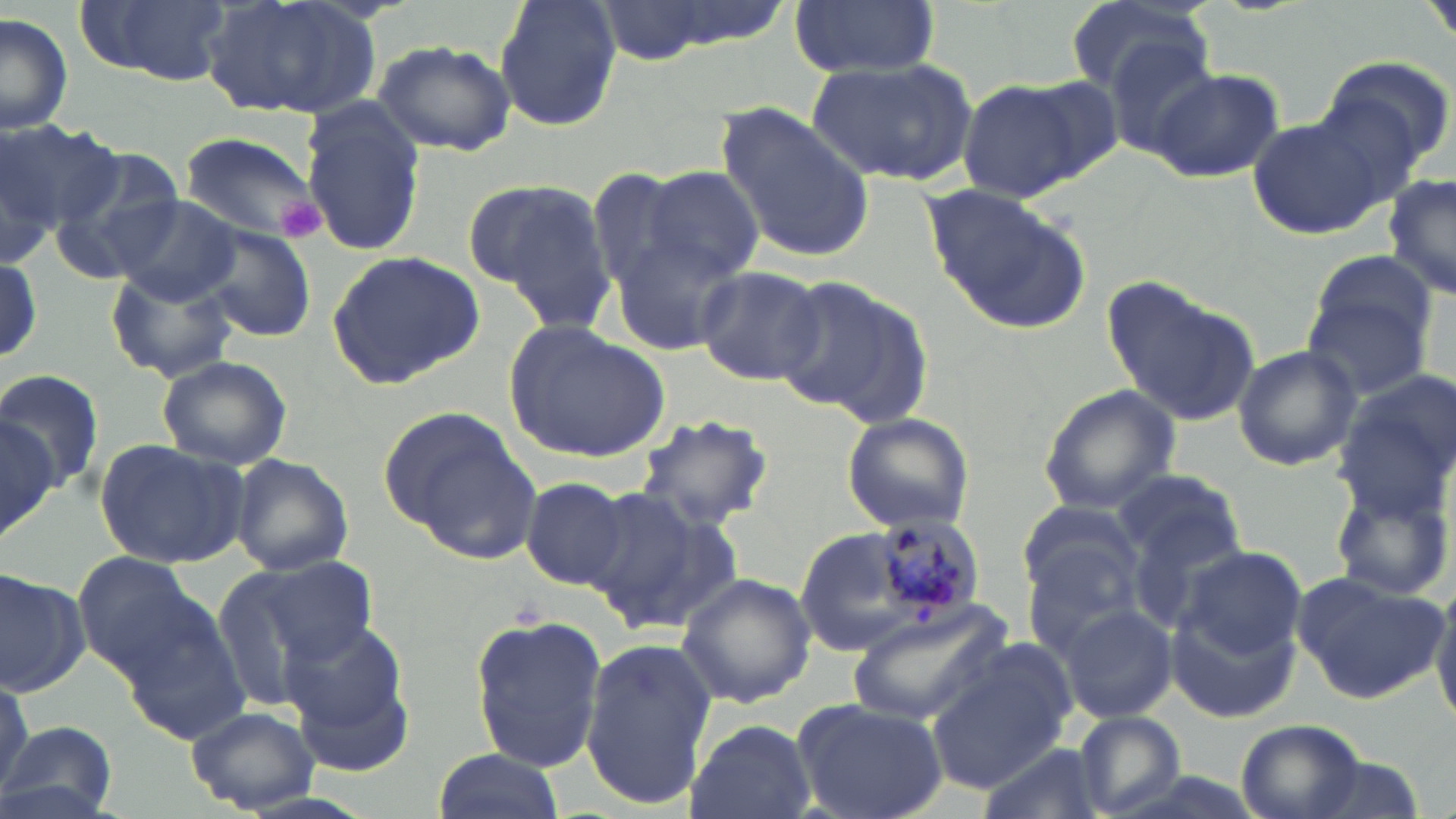
Approximate bounding boxes as (x1, y1, x2, y2) in pixels. Platelet locations: (277, 198, 328, 238). Uninfected red blood cell locations: (76, 0, 231, 86), (202, 0, 381, 123), (494, 0, 622, 132), (591, 0, 781, 63), (787, 0, 942, 79), (1064, 0, 1215, 102), (1422, 0, 1456, 46), (0, 13, 74, 135), (1102, 36, 1232, 163), (372, 40, 516, 156), (1321, 52, 1455, 175), (809, 56, 977, 187), (1145, 65, 1285, 184), (1017, 76, 1126, 182), (959, 80, 1087, 202), (298, 101, 426, 258), (713, 103, 877, 264), (1248, 116, 1389, 239), (0, 117, 118, 240), (178, 129, 326, 249), (0, 135, 58, 272), (51, 151, 190, 277), (639, 166, 765, 282), (581, 167, 704, 293), (1381, 174, 1456, 302), (470, 177, 615, 328), (920, 183, 1091, 334), (107, 193, 246, 307), (190, 223, 318, 343), (611, 232, 749, 355), (324, 250, 487, 390), (0, 252, 44, 367), (1305, 256, 1436, 392), (693, 265, 828, 387), (103, 266, 241, 384), (1104, 276, 1262, 431), (774, 278, 929, 423), (505, 321, 669, 463), (1231, 344, 1361, 470), (156, 354, 294, 471), (0, 364, 104, 496), (1330, 380, 1456, 523), (1037, 385, 1182, 515), (380, 406, 543, 559), (631, 409, 775, 535), (0, 410, 65, 530), (840, 411, 975, 534), (95, 440, 248, 569), (229, 455, 353, 576), (1112, 467, 1244, 569), (1330, 472, 1454, 604), (519, 475, 632, 589), (583, 481, 741, 635), (1017, 502, 1145, 616), (790, 524, 954, 657), (1024, 543, 1147, 658), (1177, 545, 1309, 662), (234, 551, 379, 679), (75, 555, 206, 674), (2, 569, 87, 698), (1291, 570, 1447, 704), (675, 571, 815, 709), (1432, 587, 1456, 727), (1168, 597, 1302, 722), (1058, 604, 1177, 723), (847, 606, 1009, 730), (467, 610, 609, 774), (280, 616, 415, 752), (581, 635, 717, 808), (927, 648, 1072, 790), (0, 673, 32, 797), (793, 698, 950, 819), (188, 703, 317, 814), (1072, 709, 1186, 819), (682, 717, 817, 819), (1235, 719, 1367, 819), (0, 720, 121, 819), (975, 742, 1100, 819), (431, 749, 564, 819). Plasmodium malariae-infected red blood cell locations: (873, 513, 984, 622). Slide-level diagnosis: Plasmodium malariae. Thin blood smear. May-Grünwald-Giemsa-stained preparation. 1000x magnification. Light microscopy. Image is 1456×819 pixels. One field of a larger specimen.